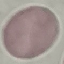

Summary:
  - Result: no malaria parasites detected
  - Preparation: thin blood smear
  - Capture: smartphone through the microscope eyepiece
  - Image type: cell patch, automatically extracted from a larger field of view and resized to 64 × 64 pixels
  - Stain: Giemsa